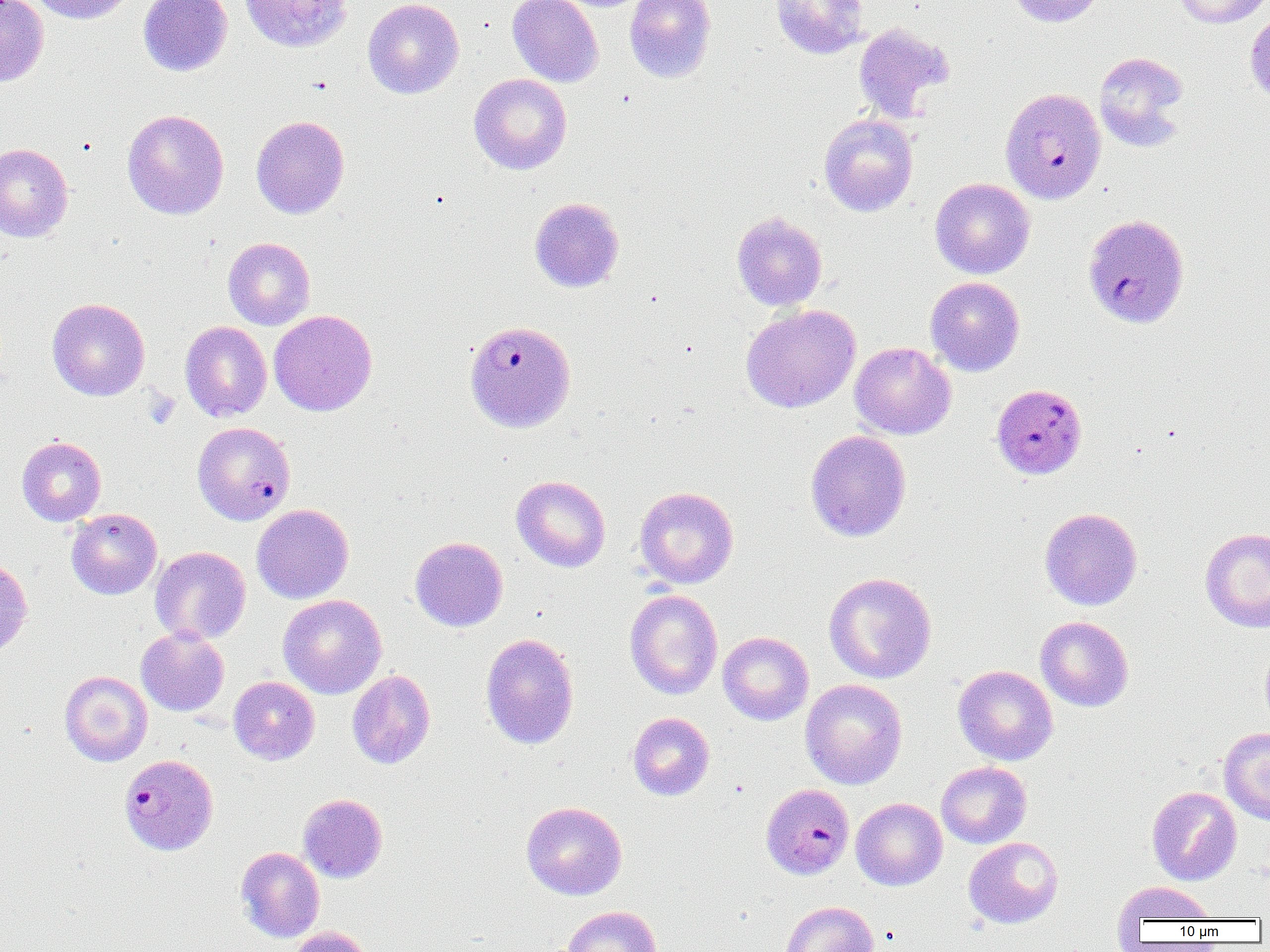

slide-level diagnosis = Plasmodium falciparum
preparation = thin blood smear
magnification = 1000x
image size = 1270×952 pixels
field of view = single
modality = light microscopy
uninfected red blood cell locations = approximate bounding boxes as named x1/y1/x2/y2 corners in pixels: (x1=28, y1=0, x2=137, y2=25), (x1=138, y1=0, x2=232, y2=76), (x1=240, y1=0, x2=353, y2=52), (x1=363, y1=0, x2=465, y2=99), (x1=507, y1=0, x2=603, y2=87), (x1=624, y1=0, x2=716, y2=83), (x1=770, y1=0, x2=870, y2=59), (x1=1006, y1=0, x2=1105, y2=27), (x1=1172, y1=0, x2=1268, y2=28), (x1=0, y1=1, x2=49, y2=86), (x1=1244, y1=8, x2=1270, y2=104), (x1=853, y1=23, x2=955, y2=122), (x1=1093, y1=51, x2=1191, y2=152), (x1=470, y1=73, x2=572, y2=174), (x1=122, y1=109, x2=229, y2=220), (x1=819, y1=114, x2=918, y2=216), (x1=251, y1=115, x2=350, y2=219), (x1=0, y1=143, x2=73, y2=242), (x1=930, y1=177, x2=1035, y2=279), (x1=529, y1=197, x2=624, y2=293), (x1=731, y1=211, x2=828, y2=311), (x1=223, y1=237, x2=315, y2=330), (x1=925, y1=276, x2=1025, y2=376), (x1=46, y1=298, x2=150, y2=401), (x1=740, y1=304, x2=861, y2=413), (x1=269, y1=310, x2=378, y2=416), (x1=180, y1=321, x2=272, y2=422), (x1=849, y1=342, x2=956, y2=439), (x1=805, y1=430, x2=911, y2=542), (x1=17, y1=436, x2=106, y2=526), (x1=511, y1=475, x2=611, y2=572), (x1=634, y1=486, x2=738, y2=589), (x1=252, y1=504, x2=354, y2=604), (x1=1039, y1=507, x2=1142, y2=610), (x1=66, y1=508, x2=162, y2=599), (x1=1199, y1=527, x2=1270, y2=633), (x1=410, y1=536, x2=508, y2=632), (x1=150, y1=546, x2=251, y2=645), (x1=0, y1=557, x2=32, y2=658), (x1=823, y1=571, x2=937, y2=684), (x1=624, y1=589, x2=723, y2=700), (x1=278, y1=594, x2=387, y2=699), (x1=1035, y1=616, x2=1134, y2=712), (x1=136, y1=627, x2=229, y2=717), (x1=718, y1=631, x2=814, y2=725), (x1=480, y1=633, x2=580, y2=750), (x1=1260, y1=641, x2=1270, y2=733), (x1=952, y1=665, x2=1058, y2=765), (x1=347, y1=669, x2=436, y2=769), (x1=60, y1=671, x2=152, y2=766), (x1=228, y1=676, x2=320, y2=765), (x1=800, y1=679, x2=908, y2=789), (x1=627, y1=712, x2=715, y2=800), (x1=1218, y1=727, x2=1270, y2=824), (x1=935, y1=761, x2=1031, y2=848), (x1=1146, y1=786, x2=1242, y2=886), (x1=298, y1=793, x2=388, y2=883), (x1=851, y1=797, x2=947, y2=891), (x1=521, y1=801, x2=627, y2=900), (x1=963, y1=836, x2=1063, y2=929), (x1=236, y1=846, x2=325, y2=943), (x1=1113, y1=881, x2=1217, y2=926), (x1=781, y1=901, x2=878, y2=952), (x1=560, y1=905, x2=662, y2=952), (x1=289, y1=926, x2=375, y2=952)
Plasmodium falciparum-infected red blood cell locations = approximate bounding boxes as named x1/y1/x2/y2 corners in pixels: (x1=999, y1=87, x2=1106, y2=204), (x1=1082, y1=213, x2=1190, y2=329), (x1=463, y1=320, x2=576, y2=433), (x1=993, y1=385, x2=1089, y2=481), (x1=193, y1=421, x2=295, y2=525), (x1=119, y1=753, x2=219, y2=855), (x1=761, y1=783, x2=854, y2=879)
platelet locations = approximate bounding boxes as named x1/y1/x2/y2 corners in pixels: (x1=144, y1=390, x2=180, y2=428)